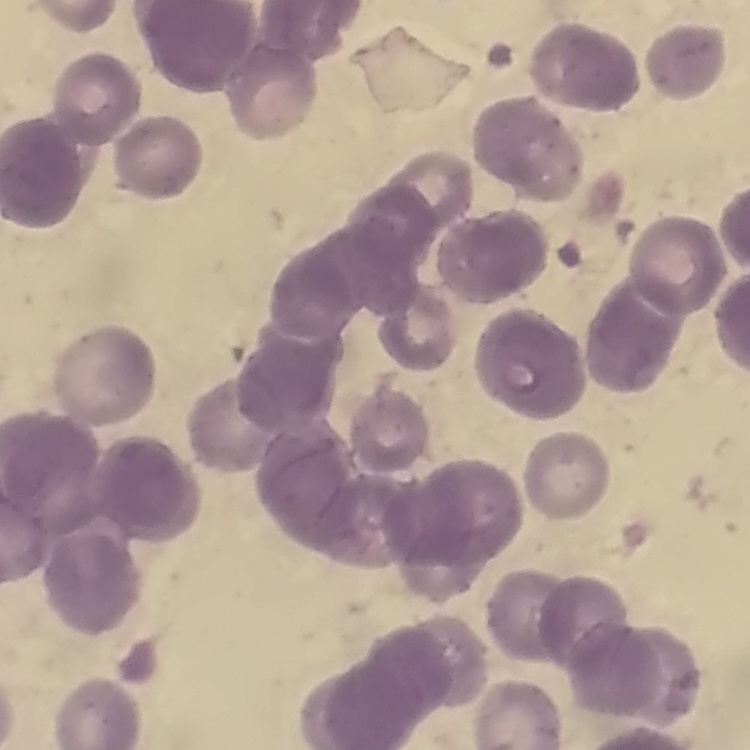

red blood cell morphology = rouleaux formation
preparation = thin blood smear
stain = Field's or Giemsa
image type = one tile cut from a larger photomicrograph